Give a bounding box for every Plasmodium parasite.
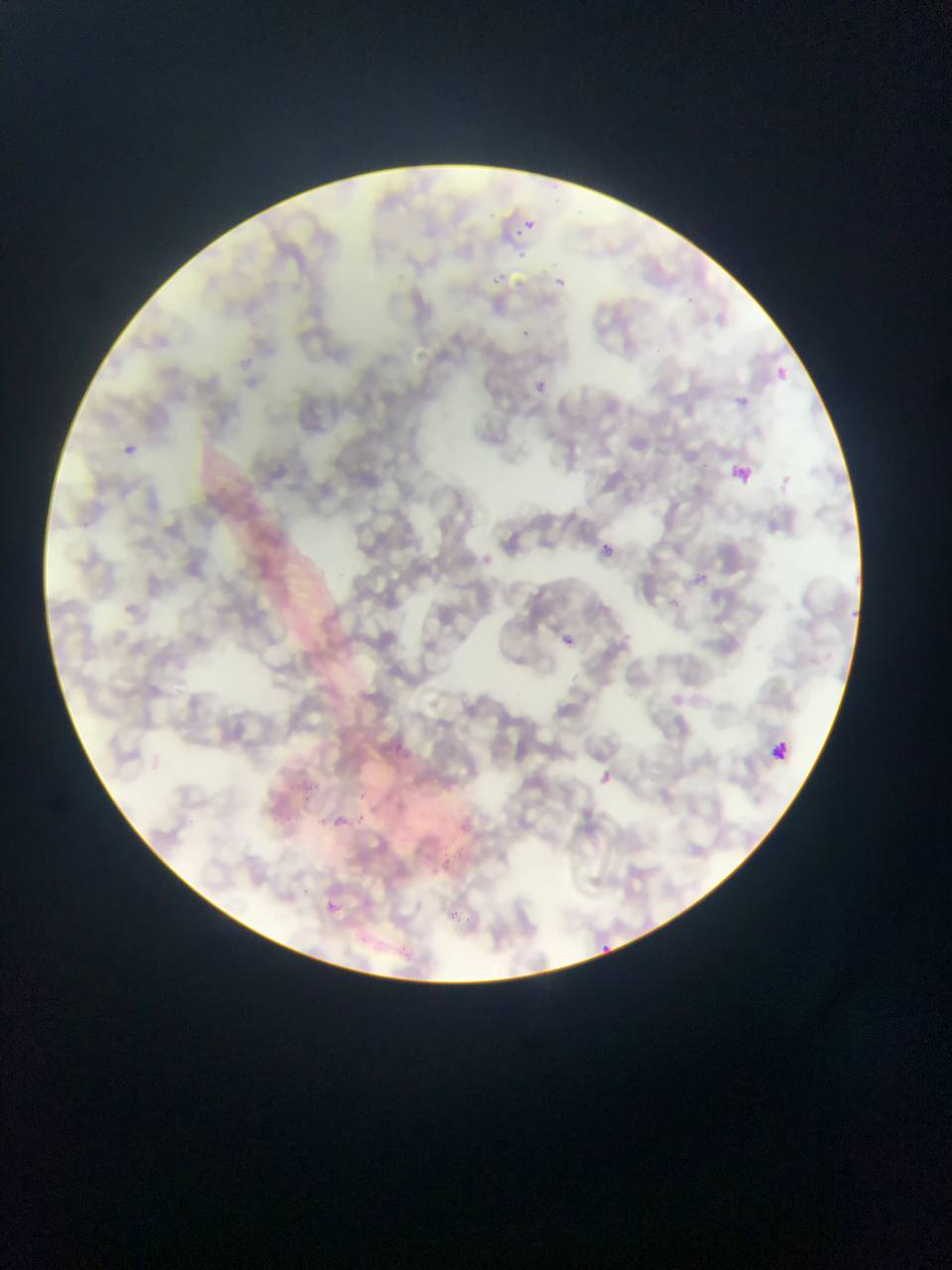

Approximate bounding boxes as (left, top, right, bottom) in pixels.
Plasmodium parasites: (516, 213, 542, 244), (481, 265, 521, 295), (552, 268, 578, 293), (516, 316, 537, 339), (231, 346, 256, 386), (759, 354, 795, 392), (526, 359, 552, 394), (732, 382, 760, 415), (124, 444, 136, 456), (731, 459, 754, 485), (595, 526, 631, 571), (471, 534, 526, 605), (549, 622, 592, 653), (382, 731, 412, 751), (595, 756, 621, 781), (445, 802, 481, 840), (322, 807, 348, 828), (319, 888, 360, 929), (590, 939, 631, 962).

Leukocyte locations: (765, 734, 795, 762). Thin blood film. Sample from Ghana. Image is 952×1270 pixels. One field of view. Photographed through a microscope with a mobile-phone camera.